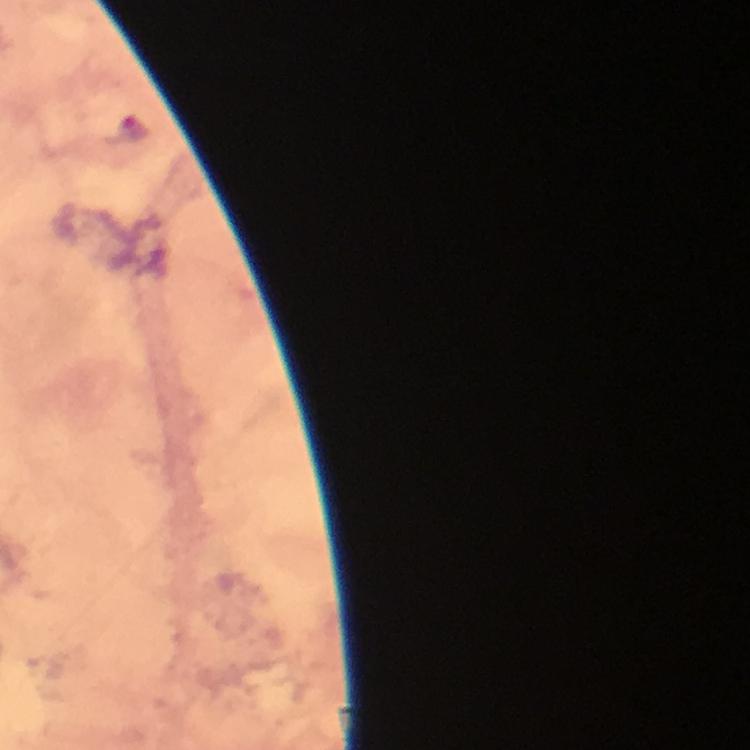

Plasmodium parasite locations = approximate centers as {x, y} in pixels: {133, 126}
capture = smartphone mounted on the microscope
preparation = thick blood smear
immersion oil = applied
stain = Giemsa
context = from a diagnostic examination for malaria
image size = 750×750 pixels
magnification = 100x
cropped from = a single field of view